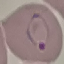

Summary:
  - Malaria status: parasitized
  - Stain: Giemsa
  - Image type: automatically extracted cell patch, resized to 64 × 64 pixels
  - Capture: smartphone through the microscope eyepiece
  - Preparation: thin blood smear